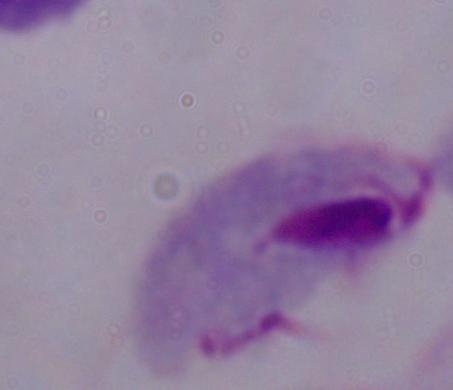

Summary:
  - Modality: photomicrograph
  - Magnification: 1000x
  - Identification: trichomonad